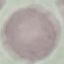
Summary:
  - Result: no malaria parasites detected
  - Preparation: thin blood smear
  - Capture: smartphone camera at the microscope eyepiece
  - Stain: Giemsa
  - Image type: cell patch, automatically extracted from a larger field of view and resized to 64 × 64 pixels